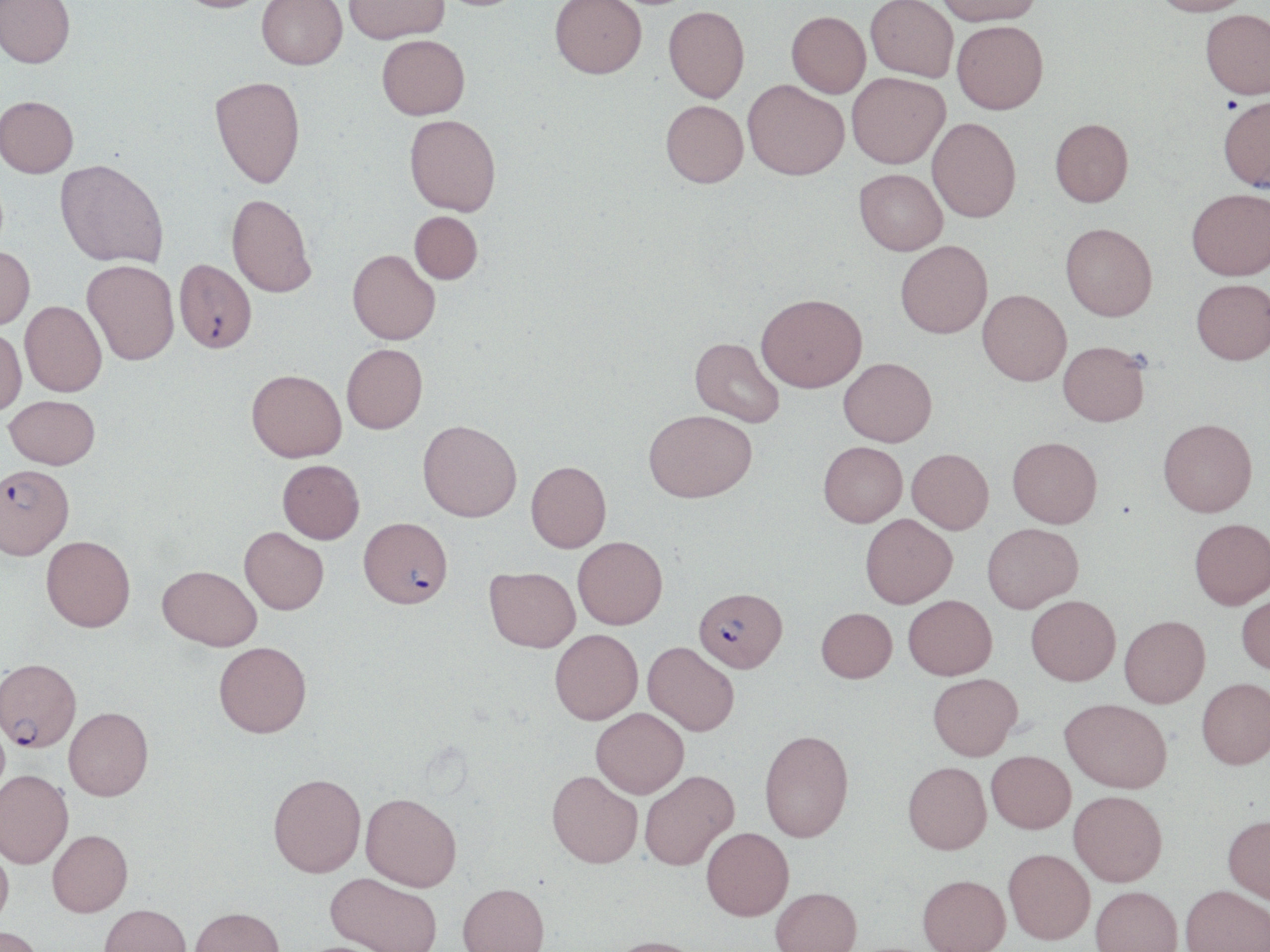

plasmodium_falciparum_infected_red_blood_cell_locations: 'approximate bounding boxes as (x1,y1)-(x2,y2) corner pairs in pixels: (175,259)-(257,354), (0,463)-(74,559), (359,516)-(452,608), (694,586)-(787,671), (0,658)-(81,751)'
slide_level_diagnosis: Plasmodium falciparum
field_of_view: one of a larger specimen
modality: light microscopy
stain: May-Grünwald-Giemsa
preparation: thin blood film
magnification: 1000x
image_size: 1270×952 pixels
uninfected_red_blood_cell_locations: 'approximate bounding boxes as (x1,y1)-(x2,y2) corner pairs in pixels: (0,0)-(75,71), (175,0)-(271,17), (257,0)-(347,73), (344,0)-(450,47), (434,0)-(529,14), (550,0)-(647,82), (865,0)-(958,85), (936,0)-(1043,30), (1150,0)-(1253,21), (663,9)-(750,106), (1200,13)-(1270,104), (786,15)-(870,100), (952,25)-(1048,119), (377,38)-(470,124), (847,75)-(950,172), (210,79)-(307,193), (743,84)-(849,185), (1217,98)-(1270,196), (0,100)-(78,180), (660,103)-(749,193), (404,117)-(501,219), (927,119)-(1021,226), (1050,122)-(1134,211), (54,162)-(168,270), (853,171)-(947,257), (1187,193)-(1270,284), (226,194)-(316,298), (409,211)-(482,284), (1060,226)-(1157,324), (896,241)-(992,339), (0,246)-(35,331), (347,249)-(440,345), (81,261)-(180,367), (1191,282)-(1270,368), (977,289)-(1070,385), (756,293)-(867,393), (20,300)-(105,398), (0,327)-(27,417), (690,337)-(785,427), (1058,342)-(1150,428), (342,343)-(428,433), (838,357)-(936,445), (246,369)-(346,461), (4,395)-(100,468), (644,409)-(757,501), (1158,418)-(1257,518), (418,420)-(522,521), (1007,436)-(1102,528), (819,442)-(907,526), (907,448)-(993,533), (277,459)-(364,543), (526,460)-(611,552), (860,514)-(957,607), (1190,518)-(1270,609), (982,522)-(1083,612), (240,526)-(329,614), (41,536)-(135,632), (573,536)-(668,628), (158,565)-(262,650), (485,566)-(580,651), (1237,591)-(1270,676), (903,595)-(996,679), (1026,595)-(1120,685), (816,607)-(896,682), (1119,615)-(1210,708), (550,629)-(643,724), (214,641)-(312,737), (643,641)-(739,735), (928,673)-(1022,759), (1197,677)-(1270,769), (1061,698)-(1172,793), (64,707)-(153,799), (591,707)-(689,797), (759,729)-(853,842), (986,750)-(1075,833), (902,761)-(991,854), (0,769)-(73,867), (547,770)-(642,868), (639,770)-(739,870), (268,773)-(366,877), (1069,790)-(1168,886), (360,792)-(462,890), (1222,814)-(1270,903), (701,827)-(794,920), (48,829)-(133,916), (0,843)-(14,929), (1003,848)-(1095,944), (325,873)-(443,952), (918,874)-(1010,952), (457,883)-(549,952), (1181,884)-(1270,952), (1091,885)-(1182,952), (770,887)-(862,952), (99,903)-(191,952), (190,906)-(284,952), (0,925)-(45,952), (607,936)-(706,952)'